State which parasite is depicted.
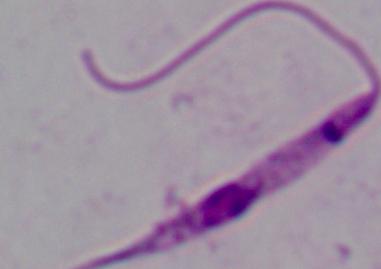

Leishmania.

Summary:
  - Modality: micrograph
  - Magnification: 1000x